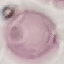
Result: negative for malaria parasites. Giemsa stain. Acquired by smartphone through the microscope eyepiece. Thin smear of blood. Automatically extracted cell patch, resized to 64 × 64 pixels.